Give the preparation type.
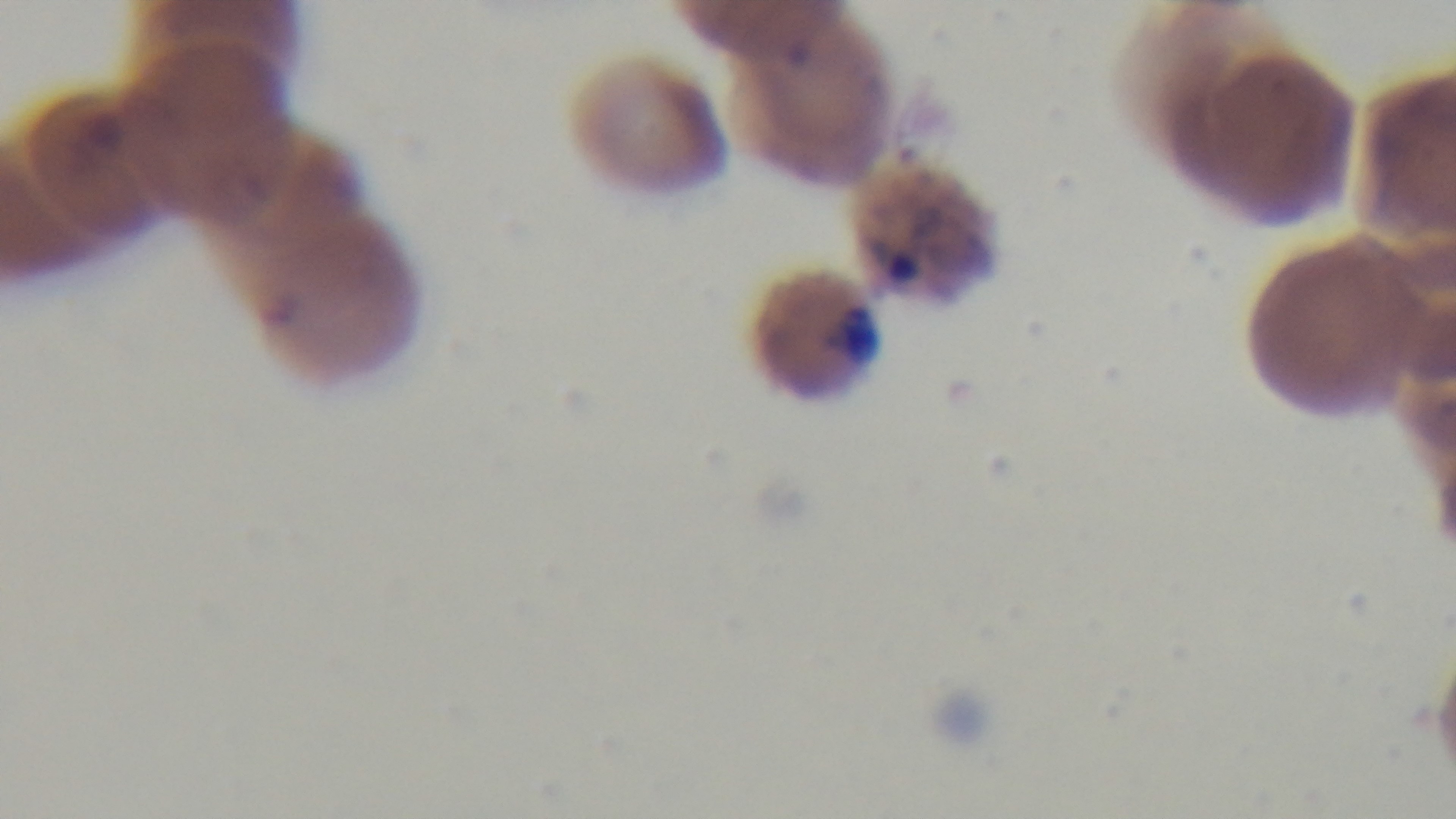
Thin.

Light microscopy. Giemsa-stained. 100x oil-immersion objective. Malaria status: infected. One field from the slide. Captured with a mounted 4K digital camera.